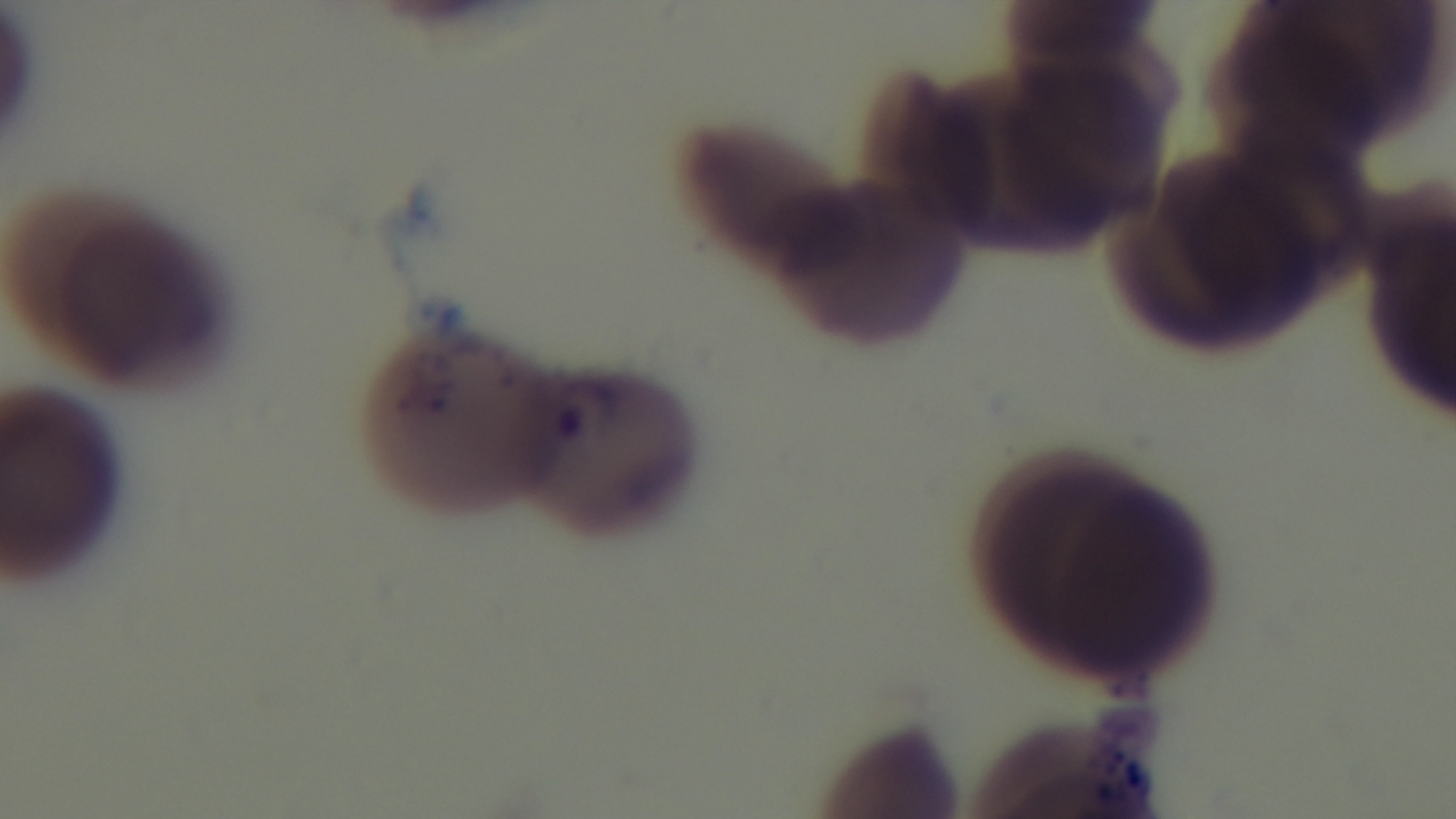

Oil-immersion objective, 100x. Single field of view. Preparation: thin blood film. Malaria status: infected. Mounted 4K digital camera. Light microscopy. Giemsa stain.